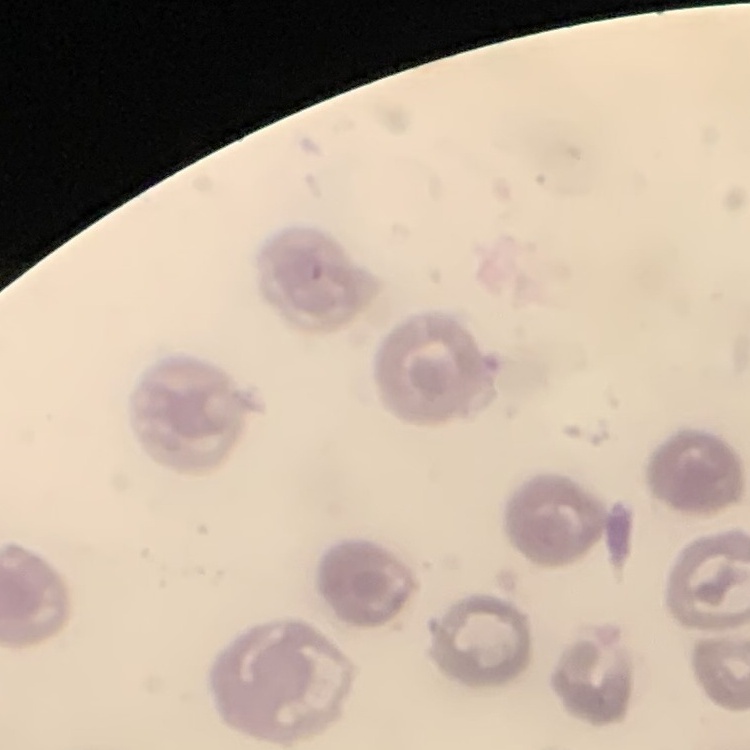
erythrocyte morphology = no rouleaux formation
preparation = thin blood smear
image type = one tile cut from a larger photomicrograph
stain = Field's or Giemsa